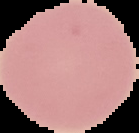

From a thin blood smear. The area outside the segmented cell region is set to black. Image is 139×133 pixels. Malaria status: uninfected.